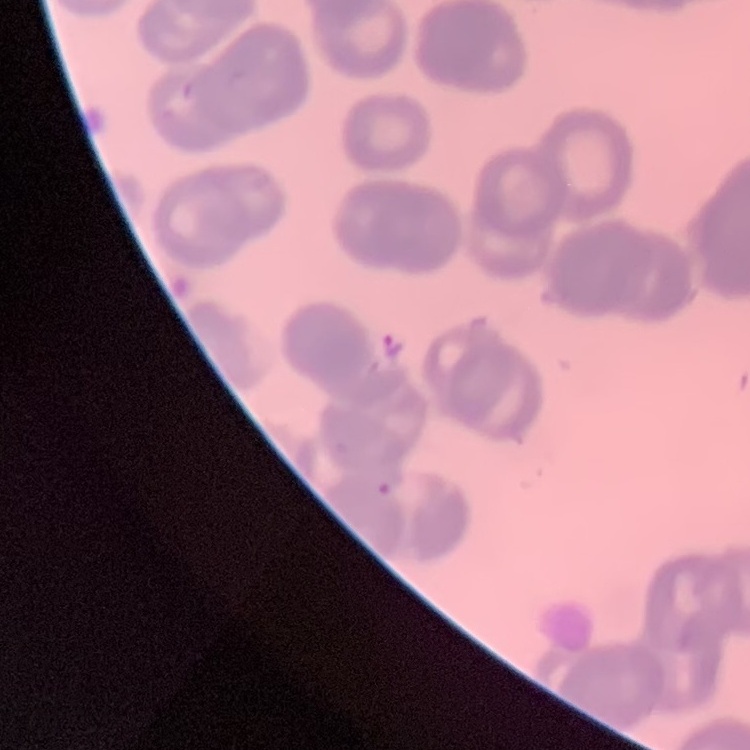
red blood cell morphology = rouleaux formation
stain = Field's or Giemsa
image type = one tile cut from a larger photomicrograph
preparation = thin peripheral smear